Assess the morphology of the erythrocytes.
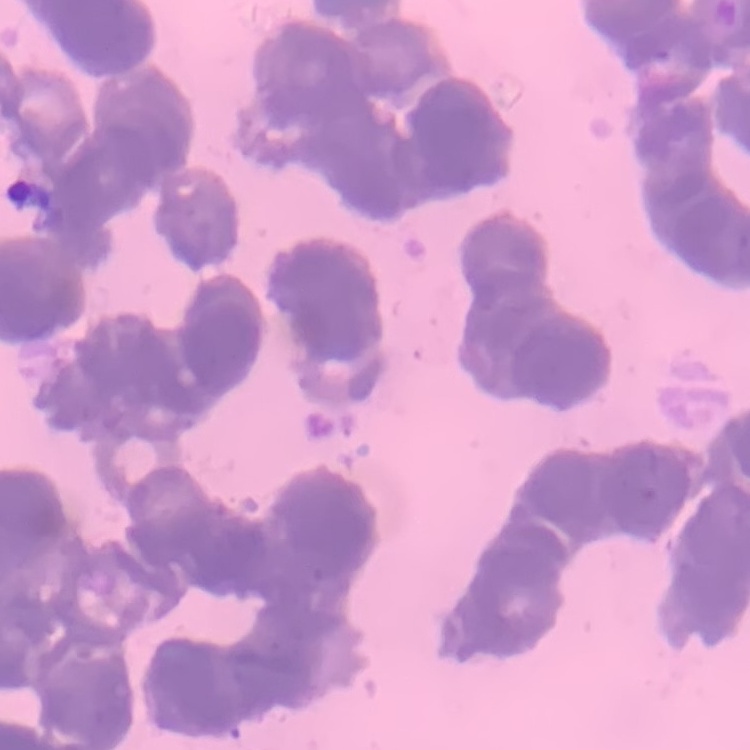

They show rouleaux formation.

preparation = thin blood smear
stain = Field's or Giemsa
image type = square crop of a larger photomicrograph